Classify this cell by malaria status.
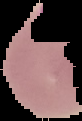

It is parasitized.

Summary:
  - Image type: segmented cell region on a black background
  - Image size: 82×121 pixels
  - Preparation: thin blood smear